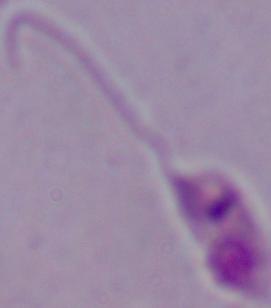
Summary:
  - Modality: photomicrograph
  - Identification: Leishmania
  - Magnification: 1000x